Classify this cell by malaria status.
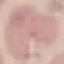
It is uninfected.

Thin blood film. Giemsa-stained preparation. Acquired by smartphone through the microscope eyepiece. Cell patch, automatically extracted from a larger field of view and resized to 64 × 64 pixels.